Identify the parasite.
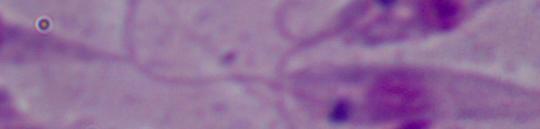
This is Leishmania.

Summary:
  - Magnification: 1000x
  - Modality: micrograph